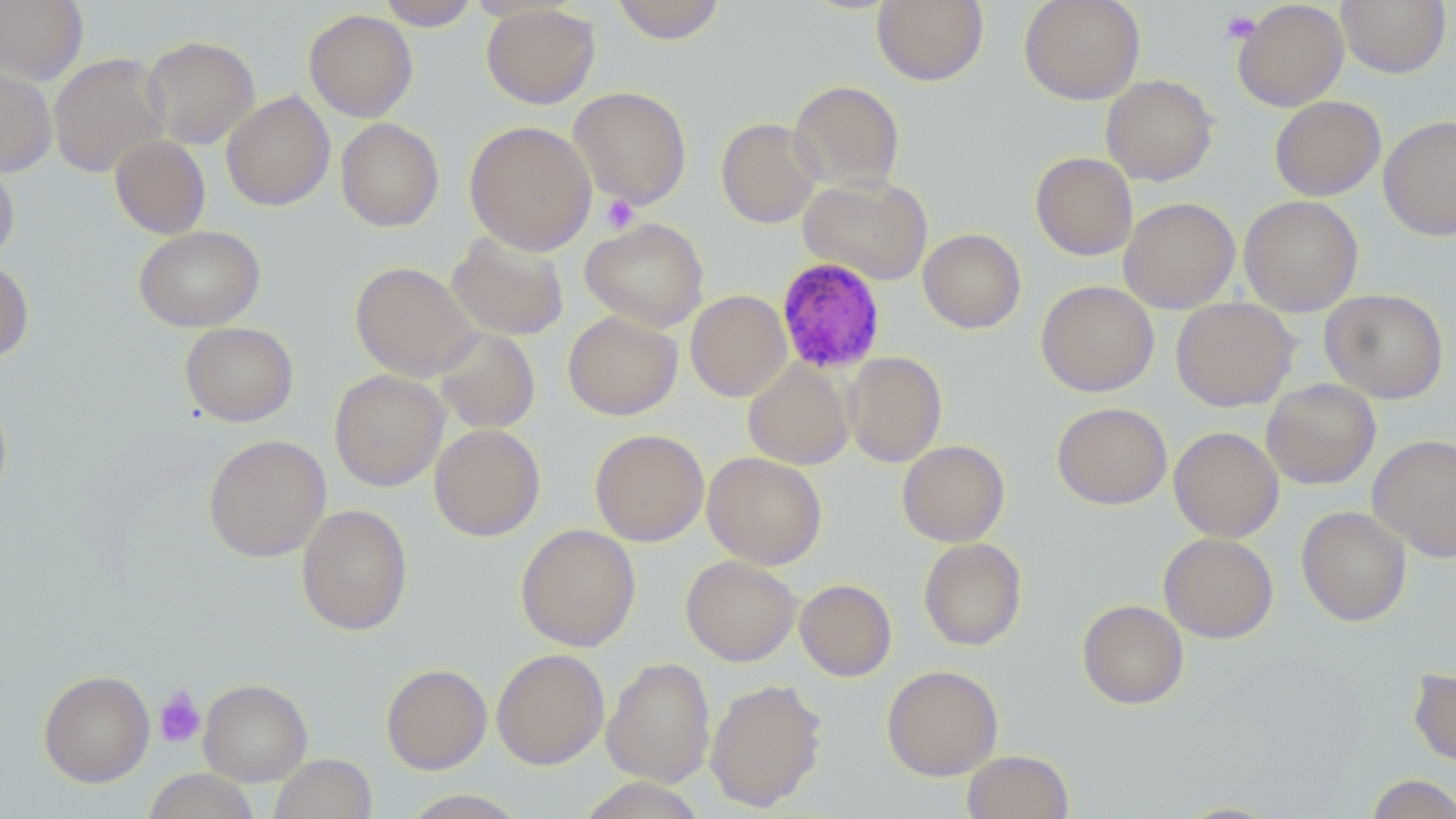
slide-level diagnosis = Plasmodium malariae
stain = May-Grünwald-Giemsa
uninfected red blood cell locations = approximate bounding boxes as (x1,y1)-(x2,y2) corner pairs in pixels: (376,0)-(481,30), (611,0)-(727,44), (872,0)-(989,86), (1019,0)-(1145,104), (1337,0)-(1450,77), (0,1)-(89,85), (1232,1)-(1349,111), (481,4)-(600,109), (304,9)-(418,122), (140,35)-(260,149), (48,52)-(169,178), (0,62)-(56,177), (1101,75)-(1218,186), (788,80)-(905,193), (569,86)-(692,209), (221,91)-(335,211), (1269,96)-(1386,201), (1379,115)-(1456,240), (336,118)-(443,231), (716,118)-(823,228), (464,121)-(596,255), (109,135)-(211,239), (1030,152)-(1138,260), (0,157)-(19,266), (798,175)-(933,286), (1239,195)-(1363,316), (1118,197)-(1240,313), (580,217)-(709,333), (133,225)-(265,332), (918,228)-(1026,333), (447,231)-(569,342), (0,259)-(34,363), (350,261)-(479,381), (1035,280)-(1159,397), (1320,288)-(1449,404), (685,290)-(792,402), (1171,297)-(1299,411), (563,311)-(682,420), (180,322)-(299,427), (433,327)-(541,434), (843,352)-(947,467), (743,360)-(854,470), (329,369)-(449,492), (1262,379)-(1381,489), (0,389)-(13,513), (1051,402)-(1172,510), (429,424)-(546,541), (1169,426)-(1284,542), (590,429)-(709,547), (203,434)-(330,562), (1367,435)-(1456,561), (897,440)-(1010,546), (702,451)-(827,570), (296,503)-(413,636), (1297,505)-(1412,626), (515,523)-(641,651), (1158,532)-(1278,643), (918,538)-(1027,651), (681,555)-(801,666), (795,578)-(897,682), (1077,599)-(1189,709), (491,648)-(609,768), (602,657)-(716,787), (381,663)-(492,774), (882,665)-(1003,780), (1408,668)-(1456,768), (38,669)-(155,787), (198,678)-(312,785), (705,678)-(827,811), (961,750)-(1074,819), (269,753)-(377,819), (143,768)-(261,819), (1364,774)-(1456,819), (576,777)-(708,819), (397,789)-(530,818), (1168,800)-(1288,818)
magnification = 1000x
image size = 1456×819 pixels
modality = light microscopy
Plasmodium malariae-infected red blood cell locations = approximate bounding boxes as (x1,y1)-(x2,y2) corner pairs in pixels: (775,256)-(887,375)
preparation = thin blood smear
field of view = single
platelet locations = approximate bounding boxes as (x1,y1)-(x2,y2) corner pairs in pixels: (1221,10)-(1261,43), (601,194)-(639,234), (154,686)-(206,748)